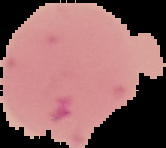
Cell region segmented out of the field of view; the surrounding area is masked to black. From a thin blood film. Result: negative for malaria parasites. Image is 166×148 pixels.